State the blood parasite species.
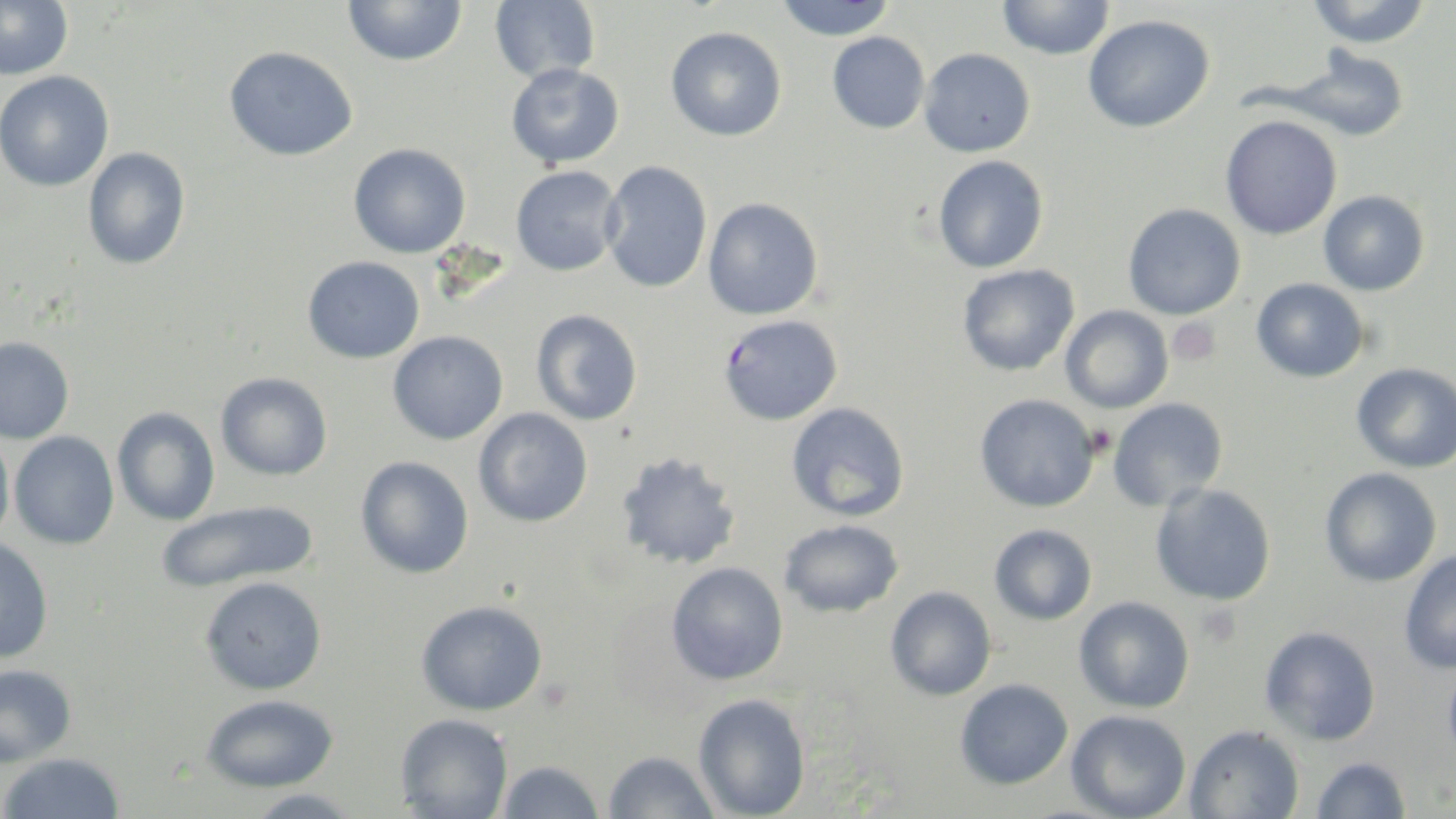
Plasmodium falciparum.

Summary:
  - Coordinate format: approximate bounding boxes as (x1, y1, x2, y2) in pixels
  - Platelet locations: (1168, 318, 1222, 367), (1085, 424, 1116, 459), (1198, 605, 1243, 649)
  - Plasmodium falciparum-infected red blood cell locations: (718, 314, 843, 426)
  - Uninfected red blood cell locations: (0, 0, 74, 80), (489, 0, 600, 84), (773, 0, 898, 40), (1305, 0, 1433, 49), (342, 1, 468, 66), (996, 1, 1116, 60), (1083, 15, 1215, 133), (665, 26, 787, 142), (827, 31, 931, 134), (224, 45, 358, 161), (919, 47, 1035, 157), (1287, 47, 1409, 142), (505, 63, 624, 168), (0, 69, 115, 191), (1220, 114, 1343, 240), (348, 143, 471, 259), (83, 147, 191, 270), (933, 155, 1049, 274), (600, 160, 712, 294), (511, 166, 623, 275), (1318, 190, 1430, 296), (703, 197, 824, 320), (1122, 202, 1246, 320), (302, 255, 425, 363), (957, 263, 1080, 377), (1251, 277, 1369, 383), (1061, 305, 1174, 413), (531, 309, 643, 425), (388, 331, 508, 445), (0, 336, 74, 444), (1351, 362, 1455, 473), (215, 372, 333, 481), (974, 393, 1100, 513), (1107, 398, 1228, 512), (786, 401, 910, 522), (112, 407, 220, 526), (473, 407, 593, 527), (0, 427, 15, 551), (9, 431, 120, 550), (616, 450, 742, 571), (356, 455, 474, 579), (1319, 467, 1442, 588), (1150, 482, 1277, 606), (155, 499, 319, 593), (779, 519, 904, 618), (989, 523, 1097, 625), (0, 537, 54, 664), (1399, 549, 1456, 675), (667, 562, 789, 684), (199, 576, 327, 695), (885, 585, 997, 701), (1074, 596, 1195, 714), (417, 600, 548, 715), (1259, 625, 1382, 746), (1442, 653, 1456, 772), (0, 662, 77, 768), (955, 678, 1073, 790), (200, 693, 339, 793), (693, 693, 811, 819), (1066, 709, 1191, 819), (394, 713, 513, 818), (1185, 724, 1305, 819), (603, 751, 721, 818), (0, 752, 125, 818), (1311, 755, 1412, 817), (496, 760, 606, 819), (244, 789, 363, 819)
  - Image size: 1456×819 pixels
  - Modality: light microscopy
  - Preparation: thin blood film
  - Stain: May-Grünwald-Giemsa
  - Field of view: single
  - Magnification: 1000x